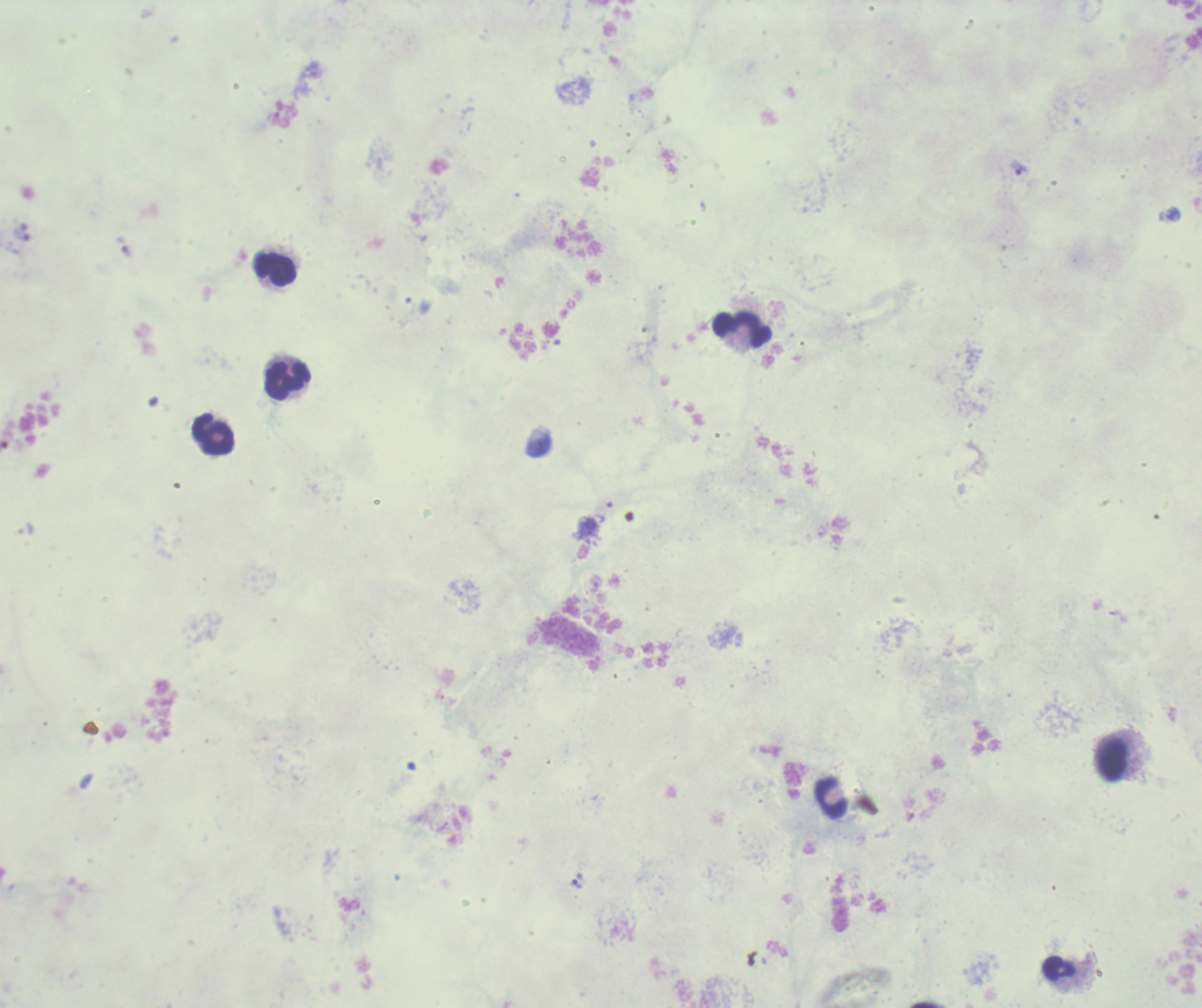
Approximate centers as {x, y} in pixels. Leukocyte locations: {276, 269}, {742, 328}, {287, 380}, {212, 435}, {1112, 758}, {832, 797}, {1059, 968}. Trophozoite locations: {1021, 170}, {127, 251}, {577, 884}. Image is 1202×1008 pixels. Romanowsky-stained preparation. Result: positive for Plasmodium parasites. Previously used in a real diagnosis. 100x magnification. Thick blood film. Single field of view. Background quality: poor.